Point out each leukocyte.
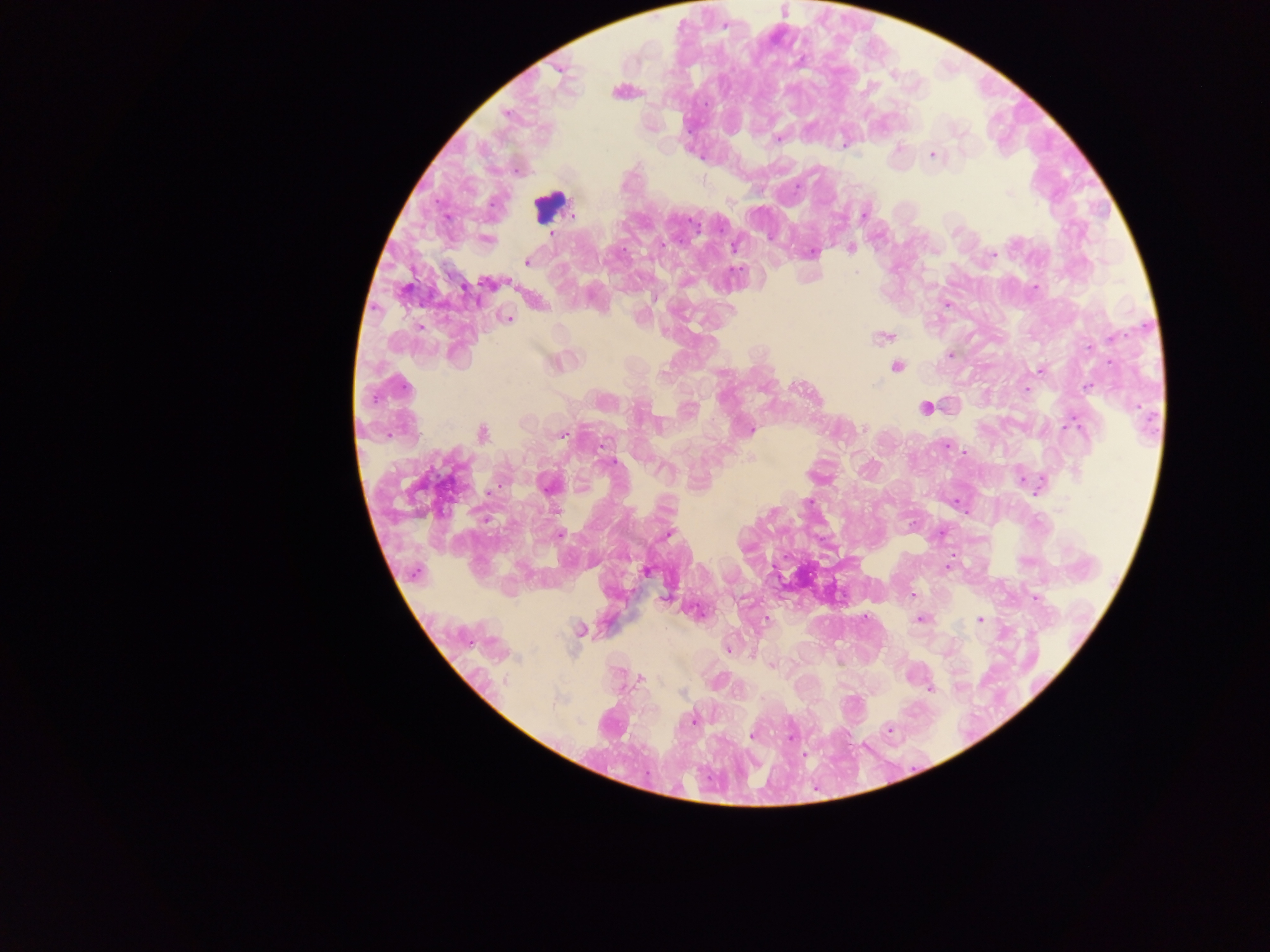

Approximate centers as (x, y) in pixels.
Leukocytes: (550, 205).

Summary:
  - Plasmodium parasite locations: (724, 25), (705, 104), (507, 114), (960, 133), (778, 139), (932, 155), (1009, 192), (573, 215), (863, 215), (695, 223), (551, 235), (735, 246), (850, 248), (811, 253), (993, 254), (527, 262), (857, 272), (487, 283), (1035, 288), (947, 304), (509, 318), (883, 336), (1112, 337), (950, 355), (896, 366), (1039, 370), (663, 374), (402, 386), (1087, 386), (1026, 389), (924, 408), (864, 428), (750, 430), (481, 434), (561, 435), (946, 444), (601, 446), (611, 461), (1022, 480), (547, 484), (809, 502), (773, 513), (668, 533), (561, 534), (947, 567), (646, 572), (416, 573), (912, 595), (1036, 598), (920, 619), (980, 619), (580, 629), (727, 650), (772, 666), (640, 678), (505, 681), (930, 690), (556, 702), (693, 719), (889, 730), (752, 736), (790, 736)
  - Capture: mobile-phone photograph through a microscope
  - Country: Ghana
  - Preparation: thick blood smear
  - Image size: 1270×952 pixels
  - Field of view: single